Point out each Plasmodium parasite.
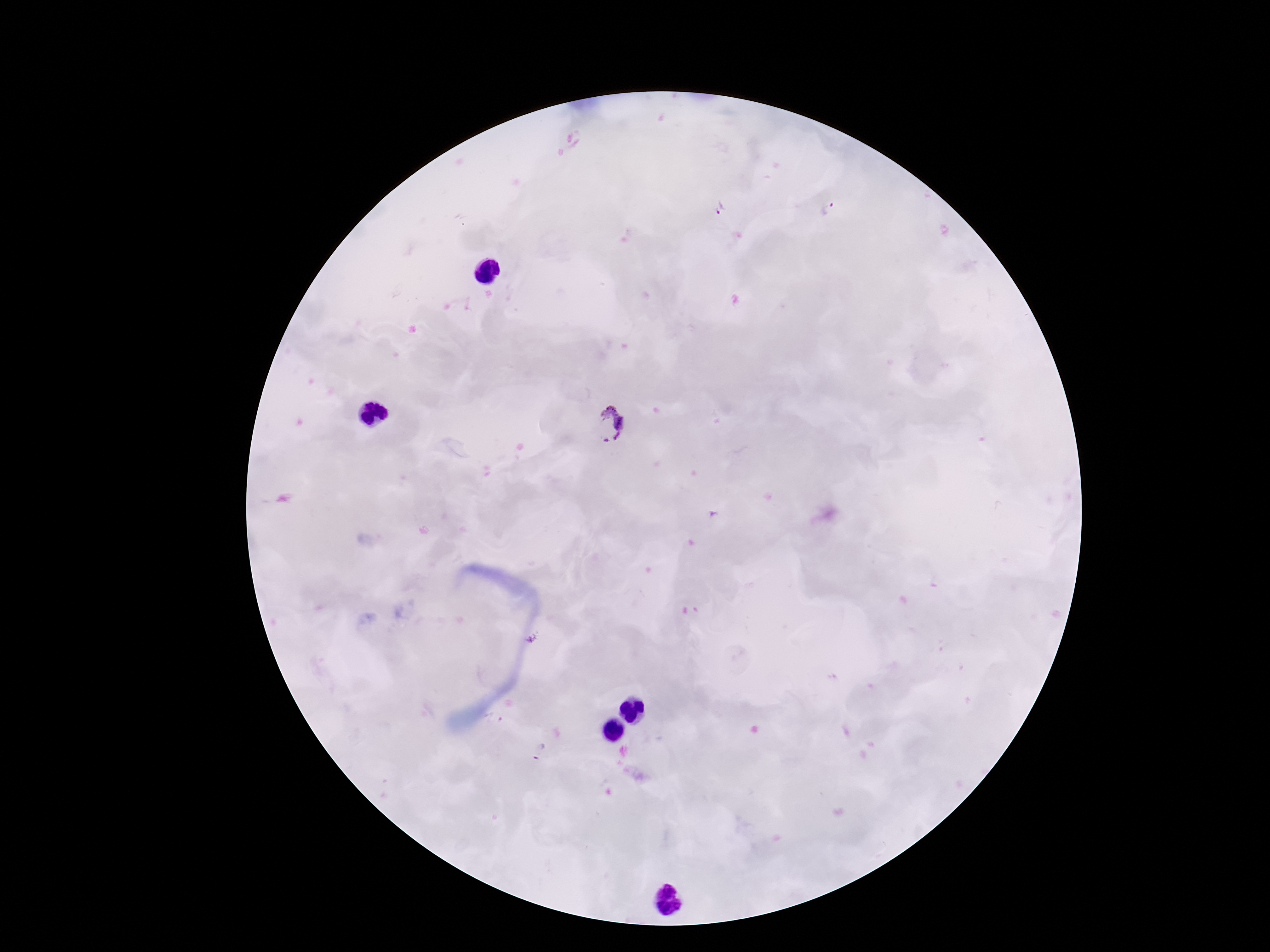

Approximate centers as [x, y] in pixels.
Plasmodium parasites: [721, 208], [828, 208], [609, 425], [495, 718], [538, 750].

100x magnification. Image is 1270×952 pixels. One field from this slide. Patient malaria status: infected. Giemsa stain. Thick peripheral-blood smear. Smartphone photograph taken through the microscope eyepiece.